Report the malaria status of this cell.
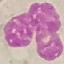
Uninfected.

{
  "image_type": "automatically extracted cell patch, resized to 64 × 64 pixels",
  "capture": "smartphone camera at the microscope eyepiece",
  "preparation": "thin blood film",
  "stain": "Giemsa"
}